Outline each Plasmodium falciparum-infected red blood cell.
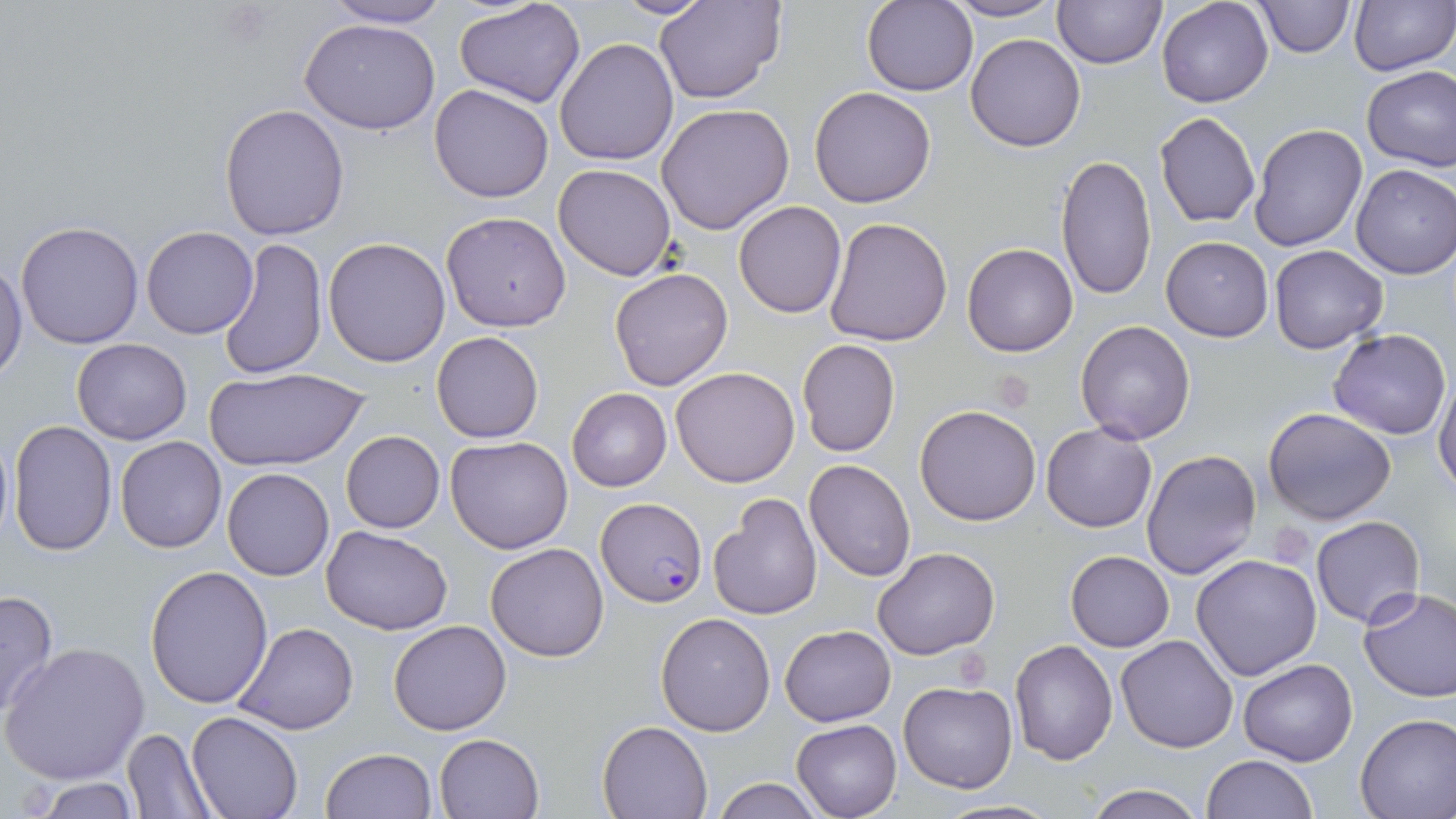
Approximate bounding boxes as [x1, y1, x2, y2] in pixels.
Plasmodium falciparum-infected red blood cells: [596, 498, 706, 606].

Summary:
  - Uninfected red blood cell locations: [322, 0, 453, 28], [613, 0, 717, 18], [655, 0, 787, 104], [1052, 0, 1167, 69], [1157, 0, 1273, 107], [1254, 0, 1353, 57], [1348, 0, 1455, 75], [456, 1, 584, 107], [863, 1, 979, 97], [943, 1, 1066, 24], [300, 18, 443, 134], [966, 33, 1086, 151], [555, 38, 678, 167], [1362, 66, 1456, 170], [429, 83, 555, 203], [808, 86, 937, 209], [219, 102, 350, 240], [656, 103, 794, 235], [1154, 112, 1261, 227], [1248, 123, 1368, 251], [1055, 153, 1158, 302], [552, 164, 677, 282], [1350, 164, 1456, 280], [734, 201, 846, 318], [441, 210, 572, 332], [825, 217, 953, 347], [15, 221, 145, 350], [142, 225, 259, 339], [1161, 235, 1274, 341], [218, 236, 327, 380], [323, 237, 451, 367], [961, 243, 1079, 357], [1268, 245, 1388, 353], [0, 257, 27, 382], [608, 266, 733, 392], [1076, 320, 1196, 444], [1330, 328, 1451, 440], [430, 330, 544, 443], [71, 338, 191, 446], [797, 338, 900, 457], [203, 366, 369, 473], [670, 366, 800, 486], [1434, 374, 1456, 496], [567, 388, 672, 492], [914, 404, 1042, 526], [1264, 407, 1396, 525], [8, 419, 117, 556], [1041, 422, 1157, 532], [1, 427, 14, 549], [340, 430, 445, 533], [116, 437, 226, 553], [445, 437, 573, 554], [1141, 448, 1261, 581], [805, 459, 915, 581], [222, 467, 333, 581], [711, 493, 821, 620], [1311, 515, 1426, 627], [321, 525, 453, 635], [484, 542, 609, 662], [872, 547, 1000, 660], [1064, 550, 1174, 651], [1192, 553, 1323, 681], [145, 565, 275, 709], [1358, 587, 1456, 704], [0, 589, 59, 721], [655, 611, 778, 737], [388, 620, 511, 736], [235, 622, 359, 735], [780, 625, 895, 727], [1115, 635, 1237, 753], [1009, 640, 1118, 765], [3, 641, 150, 785], [1238, 658, 1358, 765], [899, 681, 1017, 793], [186, 711, 303, 818], [1355, 712, 1456, 818], [793, 719, 901, 818], [598, 720, 711, 819], [122, 728, 213, 816], [434, 732, 543, 818], [320, 748, 436, 819], [1203, 755, 1317, 818], [25, 777, 140, 817], [711, 777, 826, 818], [1081, 783, 1208, 819], [933, 799, 1061, 818]
  - Slide-level diagnosis: Plasmodium falciparum
  - Image size: 1456×819 pixels
  - Field of view: single
  - Preparation: thin blood film
  - Modality: light microscopy
  - Magnification: 1000x
  - Stain: May-Grünwald-Giemsa